Give the position of every Plasmodium parasite visible.
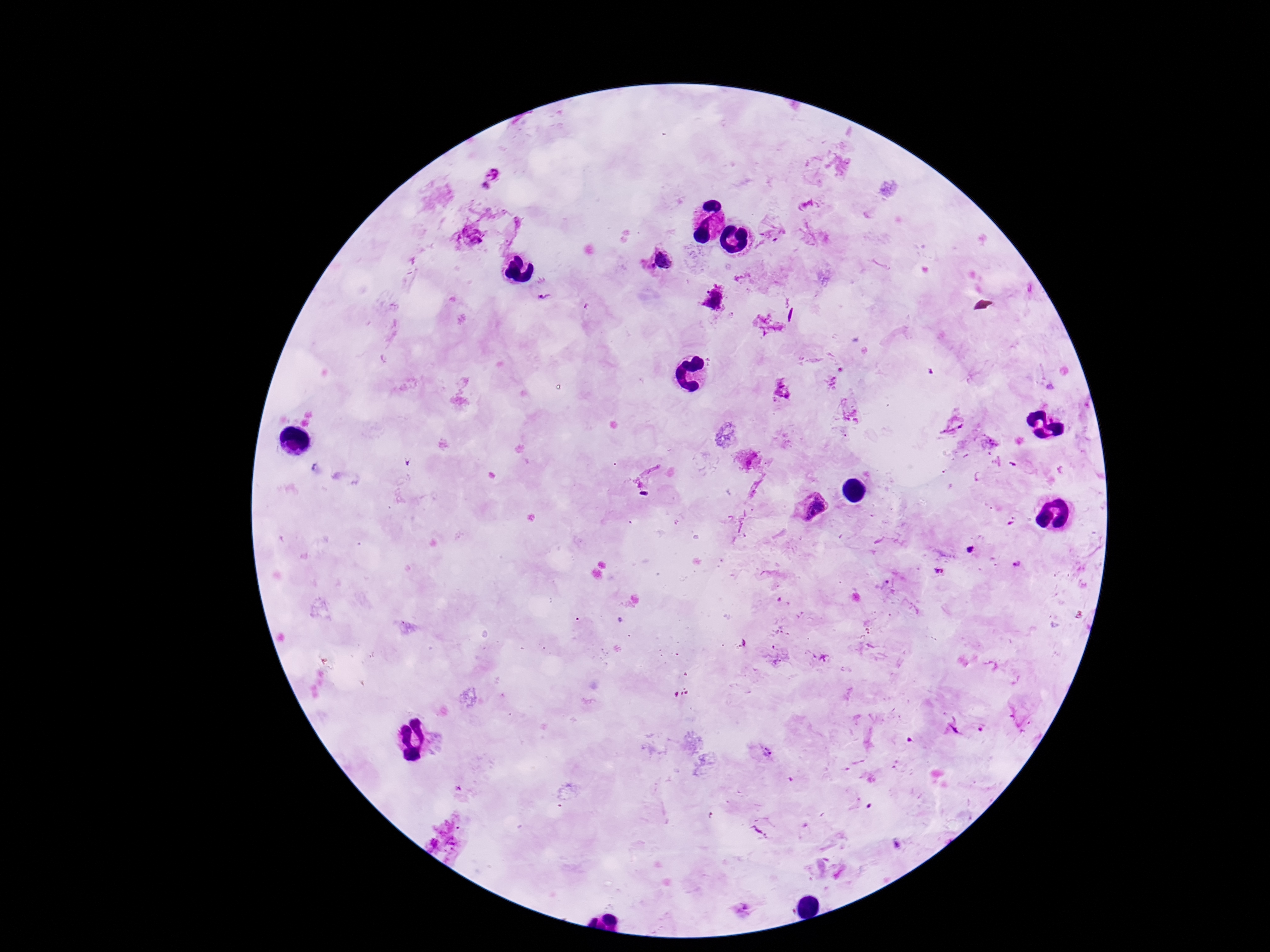

Approximate centers as [x, y] in pixels.
Plasmodium parasites: [492, 173], [661, 261], [542, 296], [713, 298], [783, 385], [812, 507], [970, 550], [1017, 563], [951, 726], [766, 751].

Summary:
  - Image size: 1270×952 pixels
  - Patient malaria status: positive
  - Magnification: 100x
  - Preparation: thick blood film
  - Capture: smartphone camera through the microscope eyepiece
  - Field of view: single
  - Stain: Giemsa